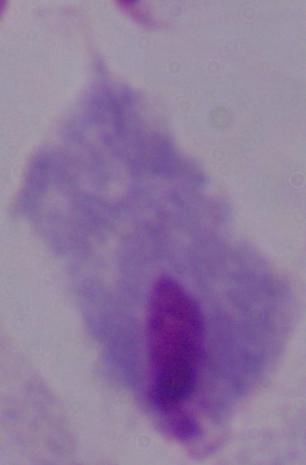
Summary:
  - Identification: trichomonad
  - Magnification: 1000x
  - Modality: photomicrograph